Comment on the morphology of the erythrocytes.
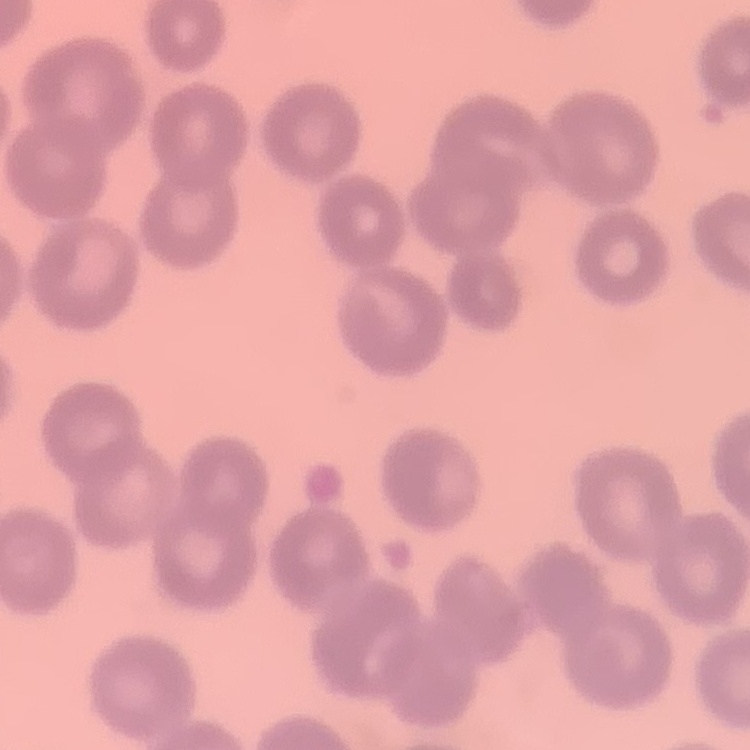
No rouleaux formation.

One tile cut from a larger photomicrograph. Thin blood smear. Field's or Giemsa stain.